Give the position of every Plasmodium parasite and every leukocyte.
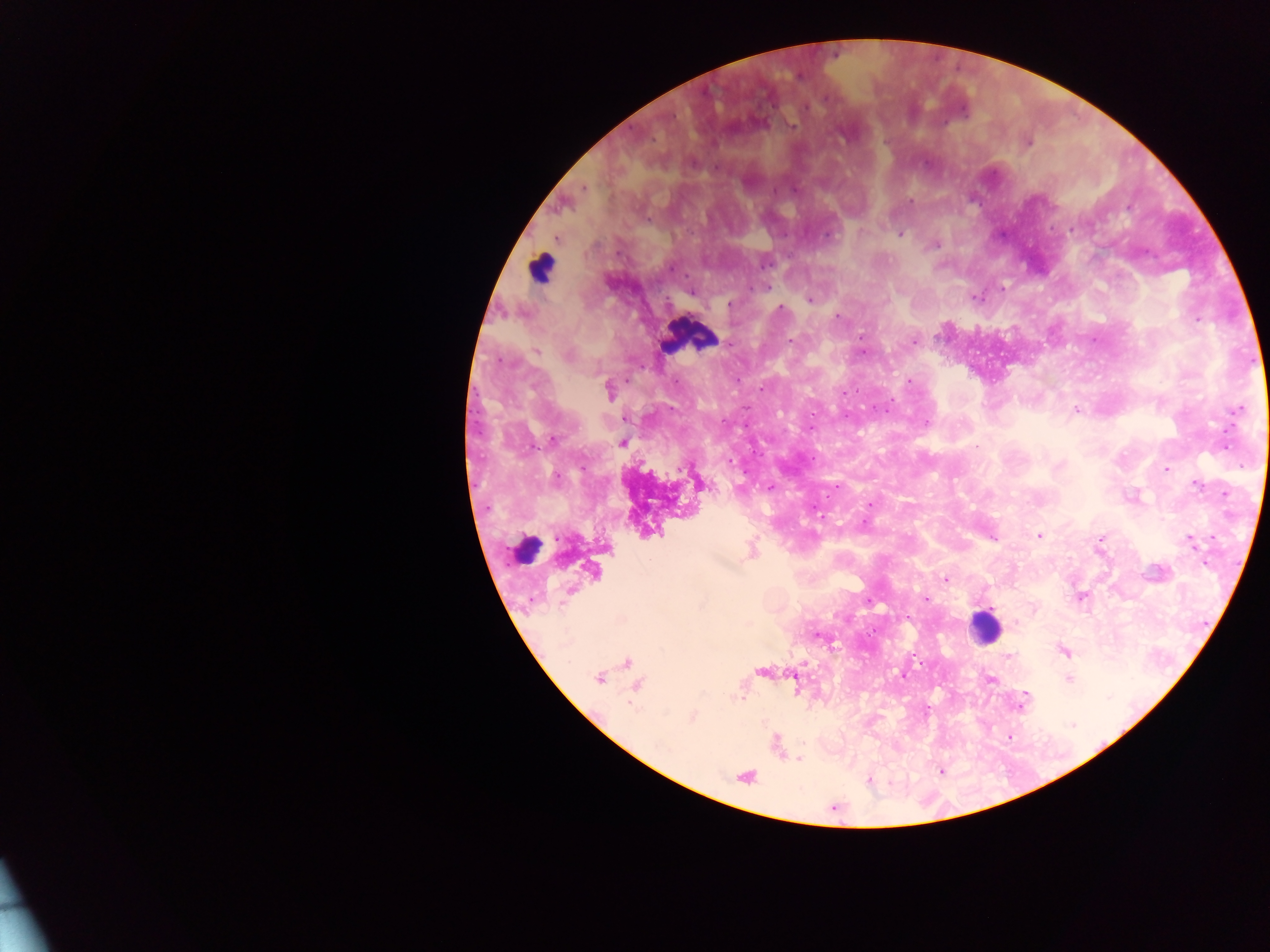

Approximate centers as (x, y) in pixels.
Plasmodium parasites: (792, 125), (1028, 142), (693, 163), (585, 189), (774, 190), (794, 190), (911, 201), (648, 221), (1070, 230), (901, 235), (828, 236), (936, 246), (765, 263), (670, 268), (768, 287), (1002, 288), (691, 292), (809, 300), (729, 304), (779, 308), (837, 316), (1197, 320), (862, 336), (791, 340), (913, 342), (536, 351), (863, 353), (910, 381), (762, 389), (610, 391), (885, 410), (1237, 410), (1076, 411), (927, 422), (553, 438), (622, 443), (977, 446), (1225, 446), (729, 461), (1166, 469), (556, 478), (1196, 485), (770, 487), (871, 504), (864, 523), (1038, 536), (1213, 536), (992, 538), (1101, 538), (1191, 542), (1205, 563), (945, 579), (870, 601), (926, 601), (907, 618), (819, 637), (1064, 651), (1008, 656), (903, 675), (598, 678), (991, 679), (1069, 679), (1023, 702), (692, 717), (1072, 724), (799, 760).
Leukocytes: (541, 267), (690, 335), (529, 548), (984, 626).

{
  "capture": "mobile-phone photograph through a microscope",
  "preparation": "thick blood smear",
  "image_size": "1270×952 pixels",
  "field_of_view": "single",
  "country": "Ghana"
}